Describe the morphology of the erythrocytes.
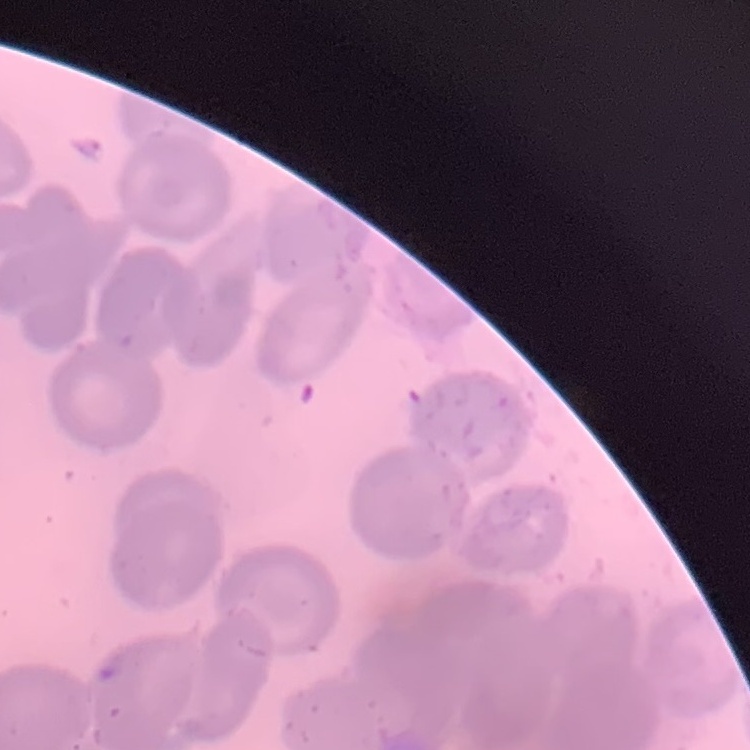

No rouleaux formation.

Summary:
  - Image type: square crop of a larger photomicrograph
  - Preparation: thin peripheral smear
  - Stain: Field's or Giemsa